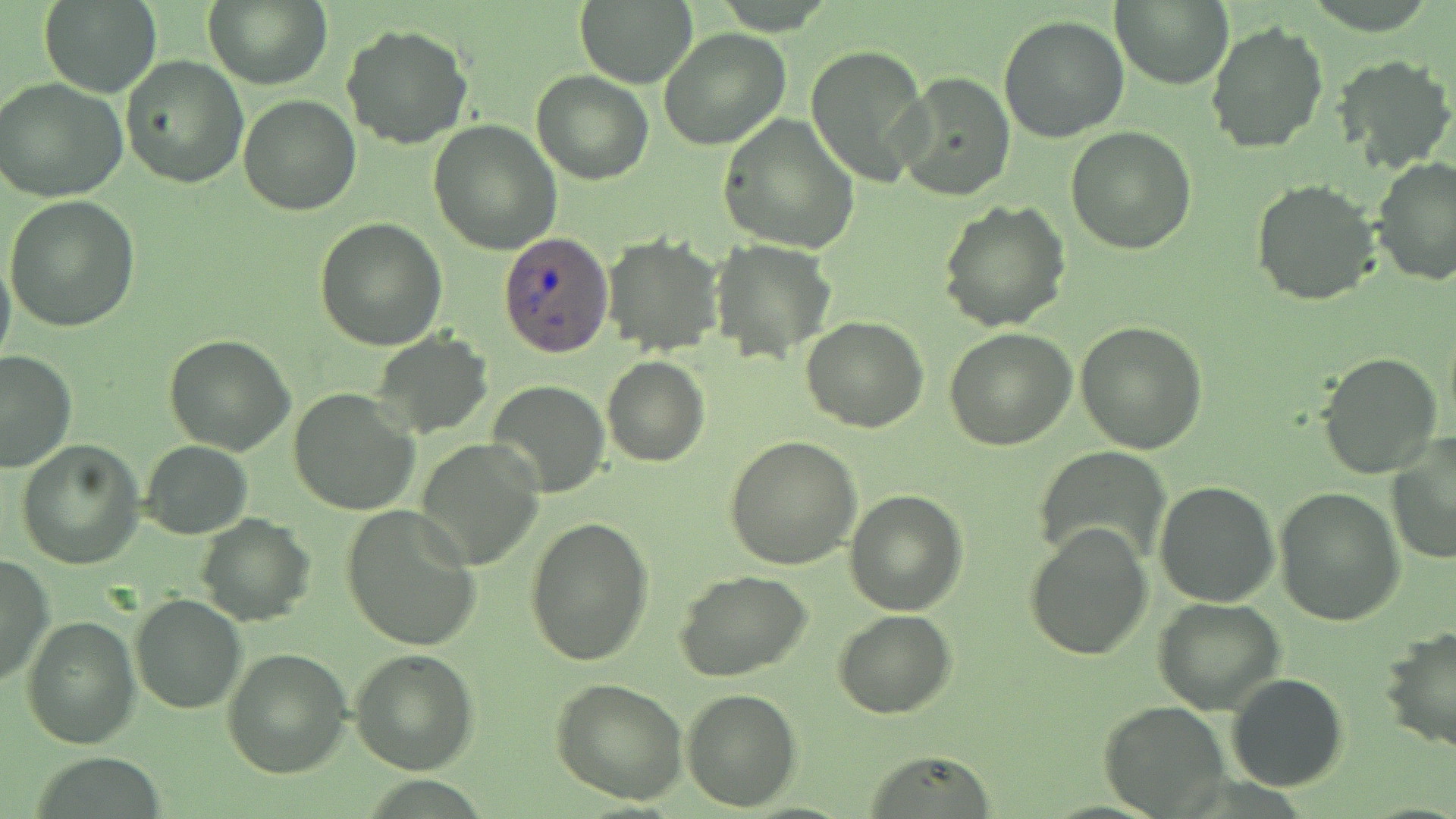
Approximate bounding boxes as (x1,y1)-(x2,y2) corner pairs in pixels. Plasmodium ovale-infected red blood cell locations: (499,231)-(614,354). Uninfected red blood cell locations: (1111,0)-(1235,91), (37,1)-(164,99), (203,1)-(331,88), (574,1)-(698,87), (998,13)-(1131,142), (1205,21)-(1327,155), (342,25)-(474,150), (658,28)-(791,152), (804,44)-(930,184), (120,56)-(249,188), (1331,56)-(1454,174), (532,69)-(653,184), (894,73)-(1016,201), (0,79)-(128,203), (238,93)-(362,215), (719,112)-(860,255), (429,120)-(562,256), (1064,125)-(1197,255), (1371,156)-(1456,286), (1250,177)-(1383,305), (5,195)-(137,331), (938,199)-(1072,331), (314,217)-(448,351), (601,234)-(724,355), (710,236)-(838,363), (0,252)-(16,375), (801,316)-(930,434), (1076,318)-(1208,454), (944,325)-(1077,449), (371,330)-(493,436), (164,335)-(296,455), (0,350)-(74,475), (1314,351)-(1445,481), (600,355)-(710,468), (488,379)-(610,496), (287,388)-(419,515), (1386,435)-(1456,566), (413,436)-(546,569), (724,437)-(862,573), (139,439)-(252,539), (16,440)-(144,569), (1035,445)-(1170,570), (1153,482)-(1280,608), (1273,487)-(1405,629), (842,488)-(967,615), (339,505)-(483,650), (195,513)-(314,625), (524,514)-(655,666), (1022,521)-(1152,663), (0,554)-(52,689), (673,571)-(813,682), (130,593)-(246,714), (1154,597)-(1286,714), (832,609)-(959,719), (21,612)-(141,749), (1379,625)-(1456,756), (349,645)-(478,776), (220,646)-(353,778), (1226,672)-(1348,792), (550,676)-(692,807), (682,686)-(801,812), (1098,700)-(1232,817), (859,749)-(997,816), (28,755)-(173,818). Slide-level diagnosis: Plasmodium ovale. Thin blood film. Optical microscopy. Image is 1456×819 pixels. Captured at 1000x magnification. One field of a larger specimen. May-Grünwald-Giemsa stain.